Report the malaria status of this cell.
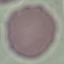

It is uninfected.

Summary:
  - Preparation: thin blood smear
  - Capture: smartphone through the microscope eyepiece
  - Stain: Giemsa
  - Image type: cell patch, automatically extracted from a larger field of view and resized to 64 × 64 pixels